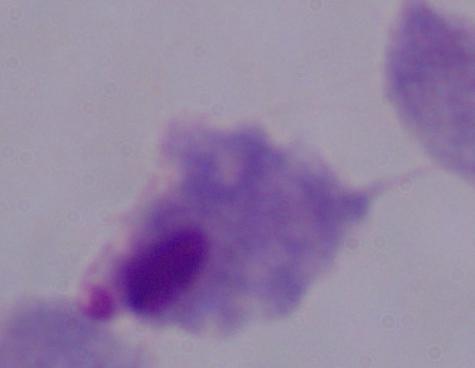
magnification = 1000x
identification = trichomonad
modality = micrograph